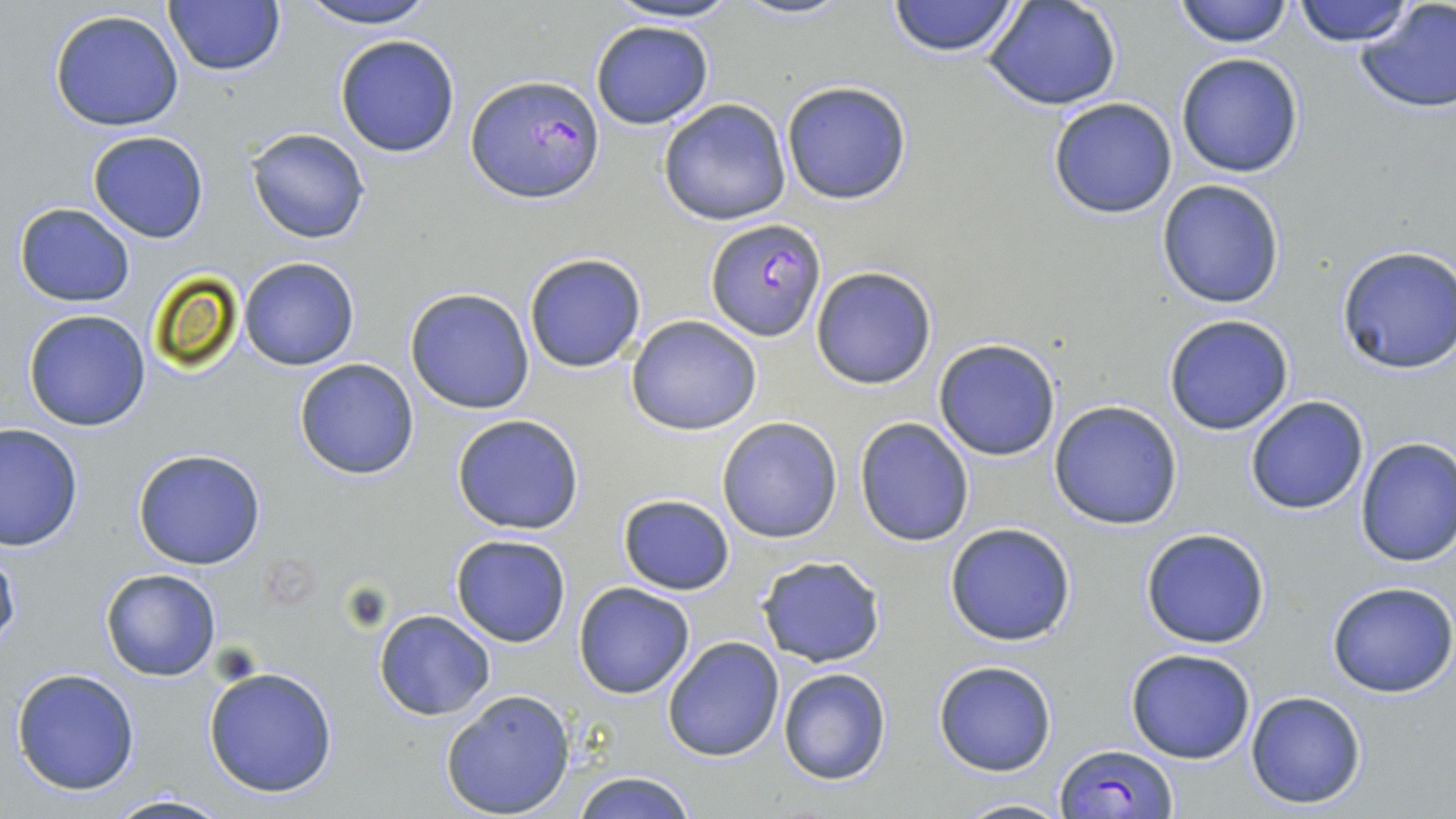 Approximate bounding boxes as [x1, y1, x2, y2] in pixels. Platelet locations: [341, 582, 396, 632]. Uninfected red blood cell locations: [292, 0, 443, 28], [602, 0, 746, 24], [734, 0, 852, 21], [886, 0, 1023, 58], [892, 0, 1112, 76], [982, 0, 1123, 112], [1173, 0, 1293, 48], [1288, 0, 1416, 48], [1352, 0, 1456, 115], [163, 1, 286, 78], [50, 8, 185, 132], [589, 20, 713, 130], [333, 33, 461, 159], [1175, 53, 1304, 178], [780, 80, 913, 205], [1048, 97, 1178, 219], [658, 98, 793, 225], [246, 128, 371, 244], [86, 130, 210, 243], [1156, 179, 1286, 309], [15, 203, 134, 307], [1335, 244, 1456, 374], [523, 251, 647, 373], [238, 257, 361, 370], [810, 266, 938, 389], [405, 287, 535, 414], [21, 310, 150, 431], [626, 314, 762, 435], [1164, 314, 1295, 436], [934, 339, 1060, 460], [294, 358, 421, 480], [1244, 395, 1370, 516], [1048, 400, 1183, 531], [451, 414, 584, 534], [854, 417, 975, 547], [716, 418, 842, 543], [0, 422, 83, 550], [1354, 437, 1456, 567], [133, 450, 266, 569], [618, 494, 736, 595], [944, 523, 1077, 646], [1139, 527, 1271, 649], [449, 534, 571, 647], [0, 547, 21, 655], [755, 555, 887, 668], [100, 569, 221, 681], [1327, 581, 1456, 697], [572, 582, 695, 699], [373, 609, 495, 720], [661, 636, 785, 761], [1125, 647, 1257, 764], [933, 661, 1057, 776], [203, 666, 340, 798], [10, 668, 141, 796], [777, 668, 892, 786], [439, 689, 577, 818], [1245, 691, 1367, 810], [568, 771, 699, 819], [105, 791, 235, 819], [954, 796, 1071, 818]. Plasmodium falciparum-infected red blood cell locations: [466, 73, 604, 204], [705, 217, 827, 341], [1056, 744, 1176, 818]. Slide-level diagnosis: Plasmodium falciparum. Thin blood smear. One field of a larger specimen. Image is 1456×819 pixels. May-Grünwald-Giemsa-stained preparation. Optical microscopy. Captured at 1000x magnification.